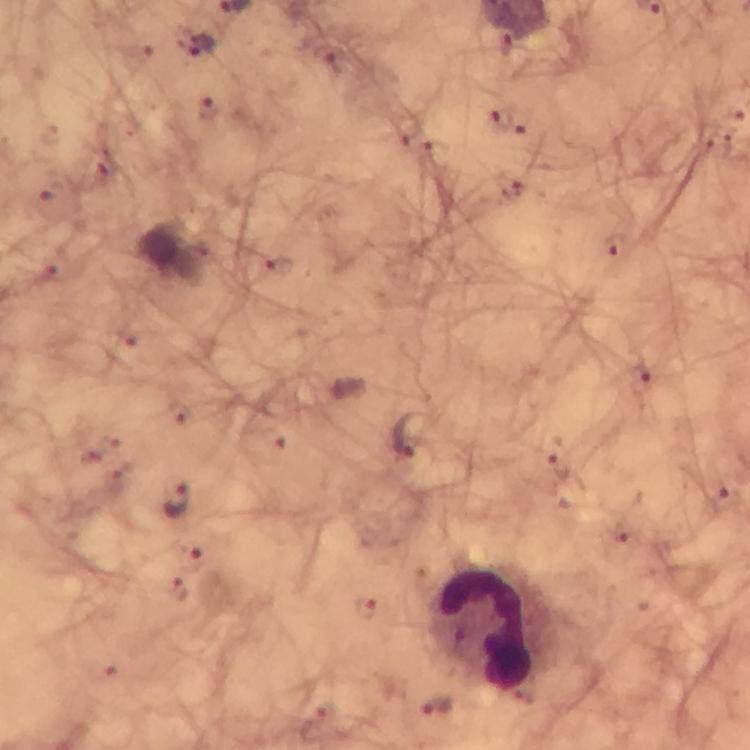

Approximate centers as (x, y) in pixels. Leukocyte locations: (494, 630). Malaria parasite locations: (199, 46), (212, 110), (501, 117), (514, 186), (616, 249), (640, 379), (410, 434), (559, 465), (727, 497), (178, 500), (194, 558), (368, 609). Thick blood smear. Immersion oil applied. Photographed through the microscope with a smartphone camera. Image is 750×750 pixels. Cropped region of a single field of view. At 100x magnification. From a malaria diagnostic workup. Giemsa stain.